Identify the cell.
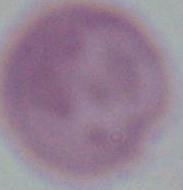

An erythrocyte.

Summary:
  - Magnification: 1000x
  - Modality: photomicrograph